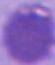
identification = red blood cell
magnification = 1000x
modality = micrograph